Identify the cell.
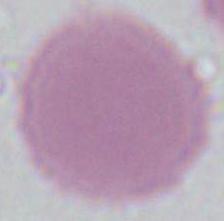
This is an erythrocyte.

{
  "magnification": "1000x",
  "modality": "photomicrograph"
}